Report the malaria status of this cell.
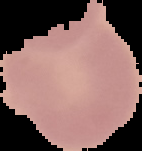

Uninfected.

From a thin blood film. Image is 142×151 pixels. Segmented cell region on a black background.